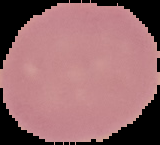

preparation = thin blood smear
malaria status = uninfected
image type = segmented cell region on a black background
image size = 160×145 pixels